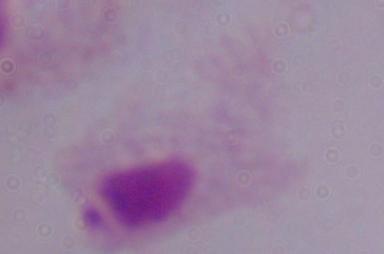

A trichomonad is shown. Micrograph. Captured at 1000x magnification.